Give the extent of all Trypanosoma brucei.
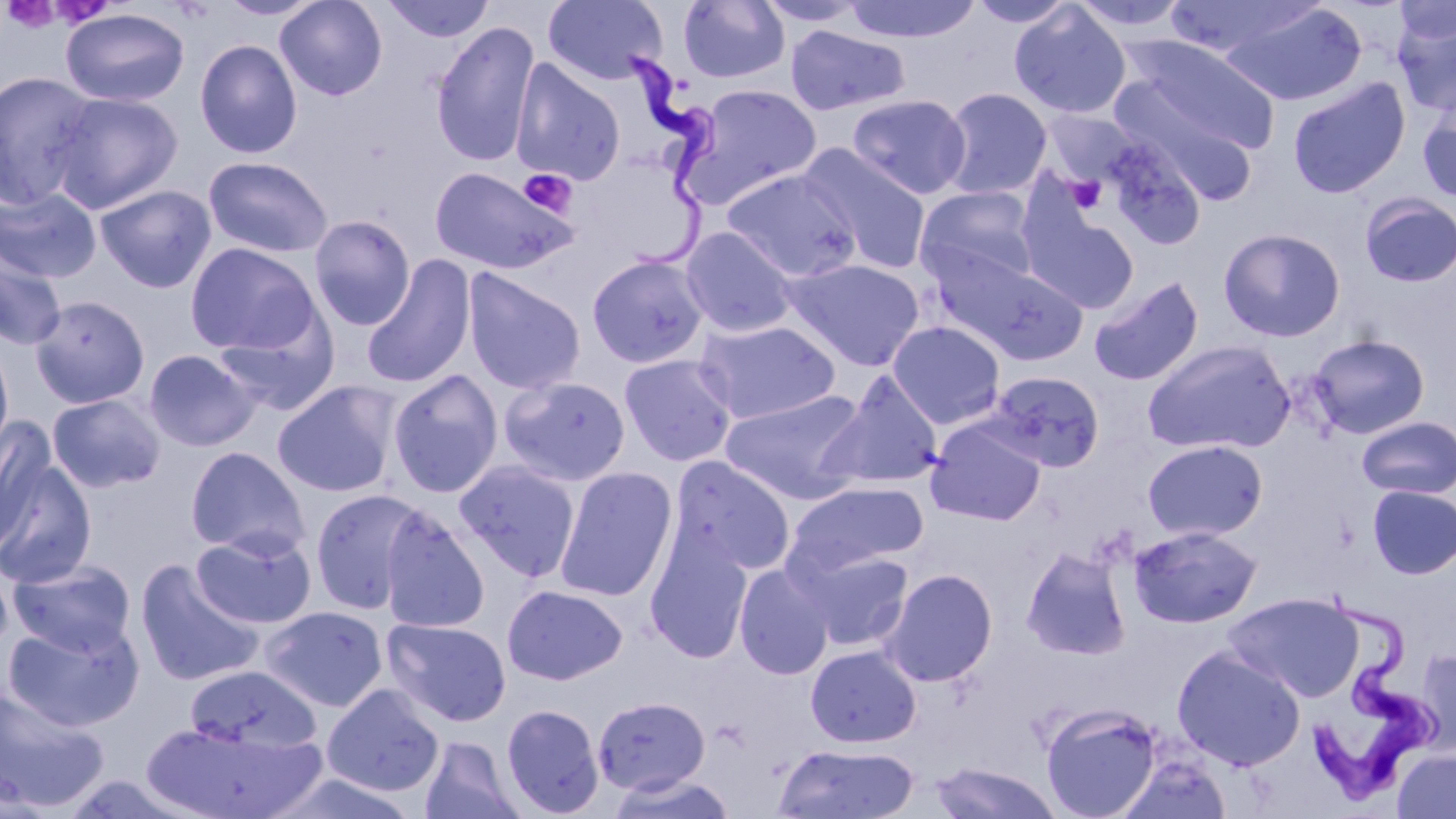

Approximate bounding boxes as [x1, y1, x2, y2] in pixels.
Trypanosoma brucei: [618, 48, 745, 278], [1296, 584, 1445, 797].

Uninfected red blood cell locations: [218, 0, 324, 21], [275, 0, 388, 101], [380, 0, 496, 43], [755, 0, 872, 28], [841, 0, 983, 43], [966, 0, 1078, 28], [1164, 0, 1325, 57], [1391, 0, 1455, 50], [542, 1, 668, 86], [677, 1, 791, 84], [1069, 1, 1194, 34], [1218, 3, 1367, 106], [1008, 4, 1131, 119], [60, 8, 190, 108], [1392, 12, 1456, 119], [431, 20, 540, 168], [785, 26, 911, 116], [1125, 36, 1282, 155], [194, 39, 303, 159], [510, 59, 626, 186], [0, 70, 100, 210], [1287, 77, 1410, 199], [1111, 82, 1260, 204], [680, 84, 823, 207], [940, 87, 1053, 199], [49, 91, 183, 213], [847, 94, 972, 199], [1418, 99, 1456, 205], [1042, 110, 1139, 190], [1100, 133, 1206, 249], [801, 146, 933, 273], [203, 156, 334, 258], [428, 165, 579, 276], [721, 170, 862, 282], [95, 184, 217, 293], [0, 186, 101, 283], [914, 187, 1040, 291], [1359, 193, 1456, 287], [1019, 199, 1139, 313], [308, 215, 416, 331], [679, 226, 800, 338], [1218, 227, 1346, 342], [185, 242, 320, 355], [0, 245, 67, 351], [929, 250, 1087, 365], [586, 254, 710, 369], [361, 255, 476, 389], [784, 258, 925, 370], [462, 268, 586, 395], [1088, 275, 1204, 387], [30, 294, 150, 409], [212, 305, 340, 416], [693, 319, 841, 424], [887, 321, 1006, 429], [1306, 334, 1430, 439], [0, 338, 14, 461], [1142, 339, 1295, 454], [143, 349, 261, 451], [618, 354, 738, 467], [387, 369, 504, 499], [984, 369, 1104, 473], [816, 374, 945, 491], [499, 375, 630, 487], [272, 381, 400, 498], [720, 389, 868, 502], [47, 393, 165, 494], [1357, 416, 1456, 500], [0, 418, 56, 553], [926, 420, 1046, 526], [1142, 439, 1268, 542], [185, 446, 310, 558], [672, 457, 796, 576], [0, 458, 97, 588], [455, 460, 581, 580], [555, 467, 677, 602], [784, 481, 928, 577], [1367, 484, 1456, 579], [308, 489, 426, 613], [379, 507, 490, 634], [1129, 525, 1262, 628], [191, 529, 317, 629], [644, 532, 753, 663], [1020, 544, 1132, 660], [795, 547, 914, 652], [8, 559, 136, 656], [134, 559, 263, 687], [733, 564, 834, 680], [881, 568, 999, 687], [502, 584, 628, 685], [1225, 593, 1362, 702], [260, 605, 388, 712], [383, 618, 512, 726], [3, 619, 144, 730], [805, 645, 921, 747], [1171, 645, 1306, 771], [1414, 649, 1455, 755], [184, 664, 320, 754], [322, 683, 445, 796], [0, 687, 110, 812], [593, 695, 710, 795], [1041, 702, 1163, 819], [501, 703, 605, 817], [141, 716, 325, 819], [419, 735, 524, 819], [772, 741, 920, 819], [1391, 747, 1456, 818], [1120, 752, 1231, 819], [928, 763, 1066, 818], [266, 769, 421, 819]. Platelet locations: [1, 1, 62, 34], [519, 169, 579, 218], [1067, 173, 1107, 214]. Slide-level diagnosis: Trypanosoma brucei. Thin blood film. One field of a larger specimen. May-Grünwald-Giemsa-stained preparation. Image is 1456×819 pixels. Captured at 1000x magnification. Light microscopy.